Name the parasite shown.
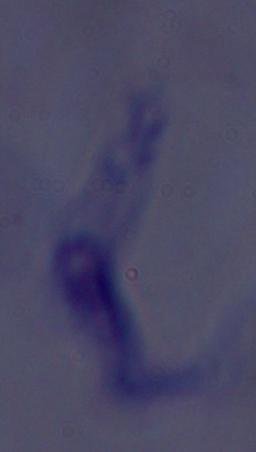
This is a trypanosome.

magnification: 1000x
modality: photomicrograph